State which parasite is depicted.
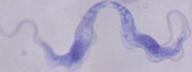

A trypanosome.

{
  "magnification": "1000x",
  "modality": "micrograph"
}